Name the parasite shown.
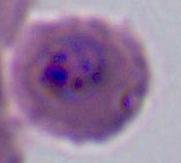

This is Plasmodium.

modality = micrograph
magnification = 400x or 1000x